Assess this cell for malaria.
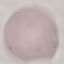

Uninfected.

image type = cell patch, automatically extracted from a larger field of view and resized to 64 × 64 pixels
preparation = thin blood smear
capture = smartphone camera at the microscope eyepiece
stain = Giemsa